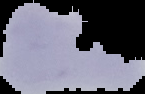 From a thin blood smear. Result: Plasmodium parasites identified. Image is 145×94 pixels. Segmented cell region on a black background.